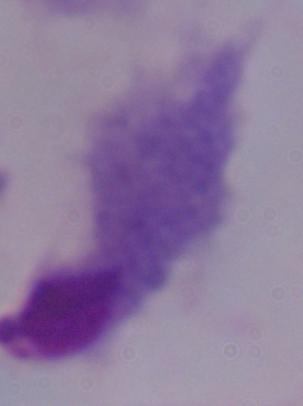

{
  "magnification": "1000x",
  "modality": "photomicrograph",
  "identification": "trichomonad"
}